Name the parasite shown.
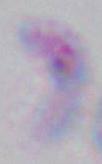
Toxoplasma gondii.

Captured at 1000x magnification. Micrograph.